Classify this cell by malaria status.
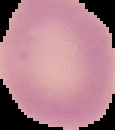

It is uninfected.

{
  "image_type": "cell region segmented out of the field of view; surrounding area masked to black",
  "image_size": "115×130 pixels",
  "preparation": "thin blood smear"
}